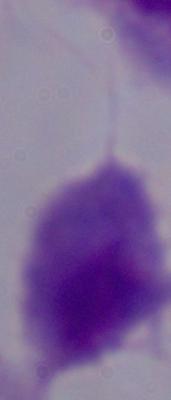 A trichomonad is seen. Captured at 1000x magnification. Photomicrograph.